Report the malaria status of this cell.
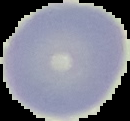

Uninfected.

The area outside the segmented cell region is set to black. Image is 130×121 pixels. From a thin blood film.